Locate and identify every blood parasite.
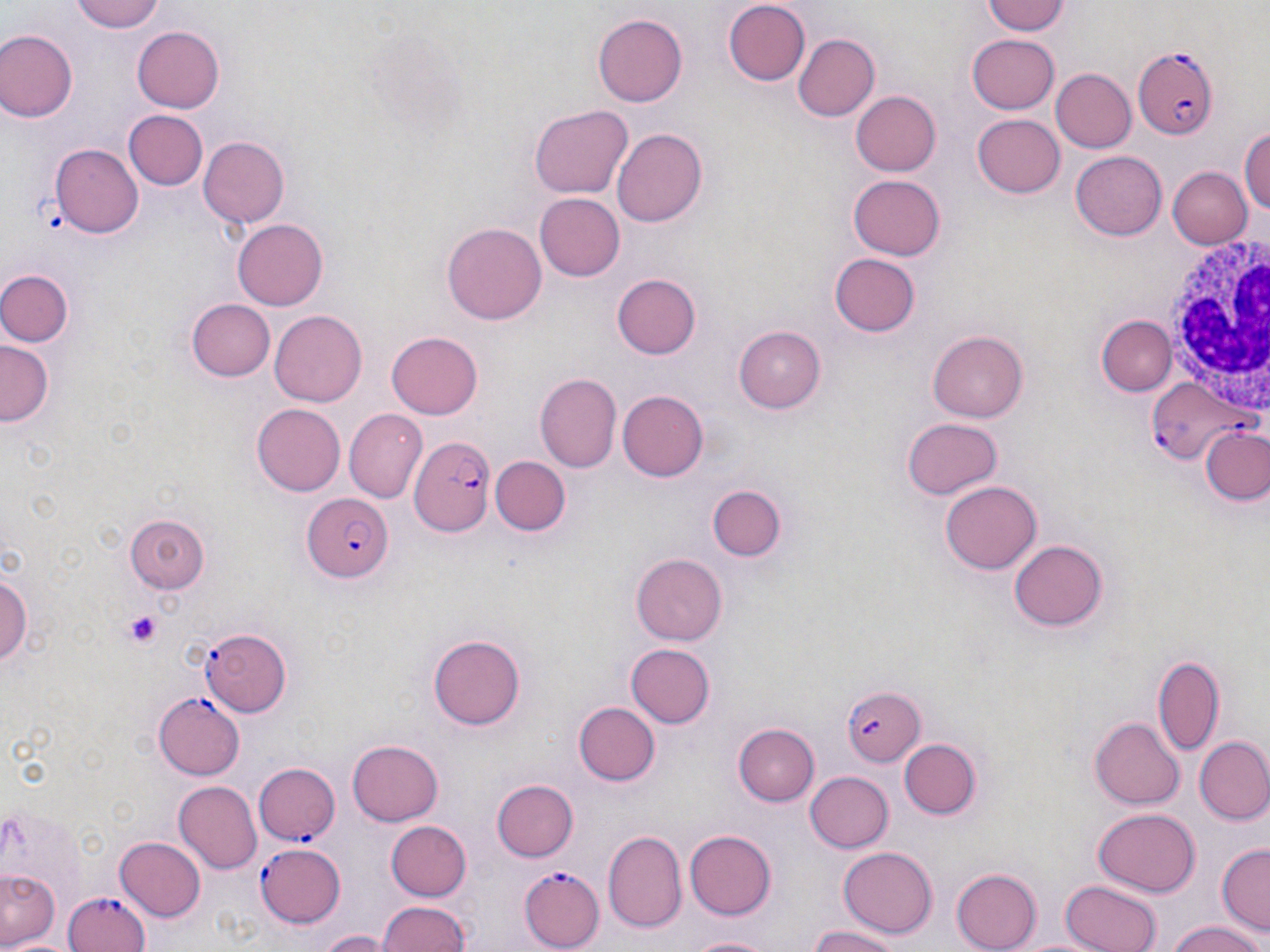
Approximate bounding boxes as named x1/y1/x2/y2 corners in pixels.
Plasmodium falciparum-infected red blood cells (subset): (x1=1131, y1=47, x2=1218, y2=140), (x1=1142, y1=374, x2=1248, y2=463), (x1=408, y1=435, x2=494, y2=537), (x1=301, y1=494, x2=394, y2=581), (x1=840, y1=686, x2=925, y2=768), (x1=153, y1=693, x2=244, y2=780), (x1=252, y1=763, x2=339, y2=846), (x1=256, y1=841, x2=348, y2=927), (x1=521, y1=866, x2=605, y2=949), (x1=57, y1=889, x2=152, y2=952).
No Plasmodium ovale, Plasmodium malariae, Plasmodium vivax, Babesia divergens, or Trypanosoma brucei observed.

Platelet locations: (x1=124, y1=612, x2=162, y2=648). White blood cell locations: (x1=1155, y1=234, x2=1270, y2=422). Uninfected red blood cell locations (subset): (x1=72, y1=0, x2=164, y2=33), (x1=981, y1=0, x2=1069, y2=37), (x1=723, y1=1, x2=811, y2=86), (x1=594, y1=14, x2=686, y2=107), (x1=132, y1=27, x2=225, y2=112), (x1=0, y1=29, x2=77, y2=121), (x1=793, y1=34, x2=877, y2=121), (x1=967, y1=34, x2=1058, y2=113), (x1=1049, y1=69, x2=1135, y2=154), (x1=851, y1=90, x2=941, y2=175), (x1=530, y1=104, x2=632, y2=198), (x1=123, y1=110, x2=208, y2=190), (x1=972, y1=114, x2=1065, y2=198), (x1=612, y1=127, x2=707, y2=226), (x1=1240, y1=127, x2=1270, y2=217), (x1=198, y1=137, x2=289, y2=230), (x1=47, y1=144, x2=143, y2=239), (x1=1202, y1=149, x2=1269, y2=247), (x1=1071, y1=151, x2=1167, y2=242), (x1=1170, y1=167, x2=1251, y2=247), (x1=848, y1=173, x2=947, y2=261), (x1=534, y1=193, x2=623, y2=279), (x1=231, y1=218, x2=328, y2=312), (x1=440, y1=223, x2=548, y2=324), (x1=831, y1=254, x2=920, y2=337), (x1=2, y1=268, x2=74, y2=347), (x1=612, y1=274, x2=701, y2=360), (x1=186, y1=297, x2=274, y2=381), (x1=270, y1=309, x2=367, y2=407), (x1=1095, y1=314, x2=1177, y2=396), (x1=736, y1=326, x2=826, y2=413), (x1=388, y1=331, x2=483, y2=418), (x1=929, y1=331, x2=1028, y2=421), (x1=1, y1=340, x2=55, y2=428), (x1=535, y1=372, x2=622, y2=474), (x1=617, y1=389, x2=709, y2=482), (x1=252, y1=402, x2=346, y2=495), (x1=345, y1=409, x2=427, y2=503), (x1=901, y1=417, x2=1001, y2=499), (x1=1203, y1=428, x2=1270, y2=508), (x1=491, y1=456, x2=571, y2=537), (x1=940, y1=480, x2=1042, y2=573), (x1=702, y1=482, x2=787, y2=564), (x1=125, y1=514, x2=207, y2=592), (x1=1008, y1=540, x2=1106, y2=631), (x1=631, y1=554, x2=728, y2=646), (x1=0, y1=559, x2=33, y2=679), (x1=428, y1=635, x2=526, y2=730), (x1=626, y1=643, x2=714, y2=728), (x1=1155, y1=656, x2=1224, y2=758), (x1=572, y1=702, x2=658, y2=787), (x1=1091, y1=716, x2=1184, y2=809), (x1=734, y1=724, x2=818, y2=805), (x1=1197, y1=736, x2=1270, y2=824), (x1=348, y1=737, x2=444, y2=826), (x1=901, y1=738, x2=982, y2=819), (x1=804, y1=770, x2=893, y2=853), (x1=491, y1=779, x2=577, y2=863), (x1=171, y1=781, x2=260, y2=873), (x1=1091, y1=807, x2=1200, y2=897), (x1=385, y1=822, x2=471, y2=900), (x1=602, y1=831, x2=686, y2=935), (x1=685, y1=831, x2=777, y2=918), (x1=114, y1=834, x2=206, y2=921), (x1=1217, y1=843, x2=1269, y2=935), (x1=838, y1=845, x2=938, y2=936), (x1=951, y1=868, x2=1041, y2=952), (x1=0, y1=869, x2=59, y2=948), (x1=1059, y1=878, x2=1164, y2=952), (x1=375, y1=900, x2=473, y2=952), (x1=1166, y1=920, x2=1266, y2=952), (x1=803, y1=925, x2=905, y2=952), (x1=316, y1=929, x2=396, y2=952), (x1=685, y1=933, x2=771, y2=952). Slide-level diagnosis: Plasmodium falciparum. May-Grünwald-Giemsa-stained preparation. Image is 1270×952 pixels. Thin blood smear. One field of a larger specimen. Captured at 1000x magnification. Light microscopy.